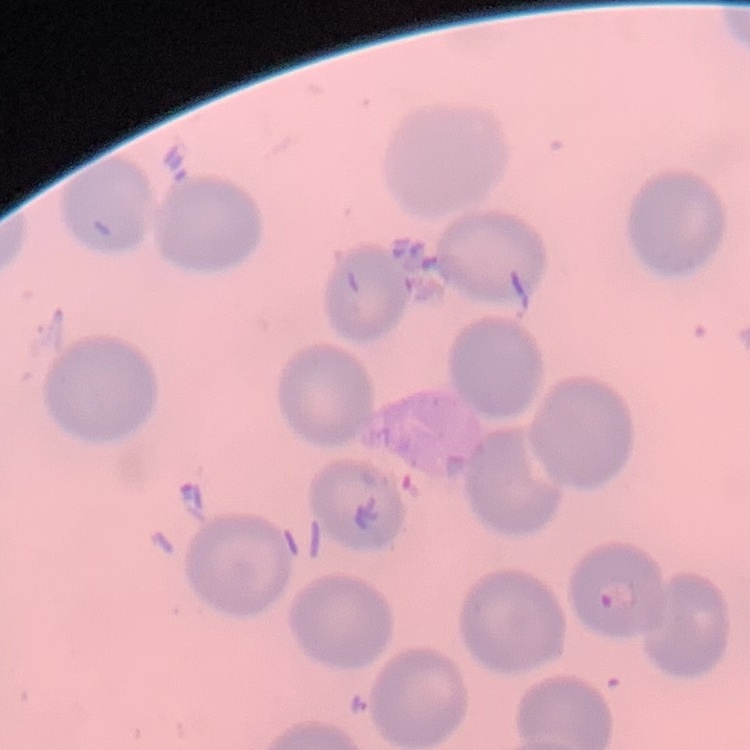

erythrocyte morphology = no rouleaux formation
stain = Field's or Giemsa
image type = one tile cut from a larger photomicrograph
preparation = thin peripheral smear